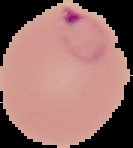
preparation = thin blood smear
result = malaria parasites identified
image size = 133×148 pixels
image type = segmented cell region on a black background